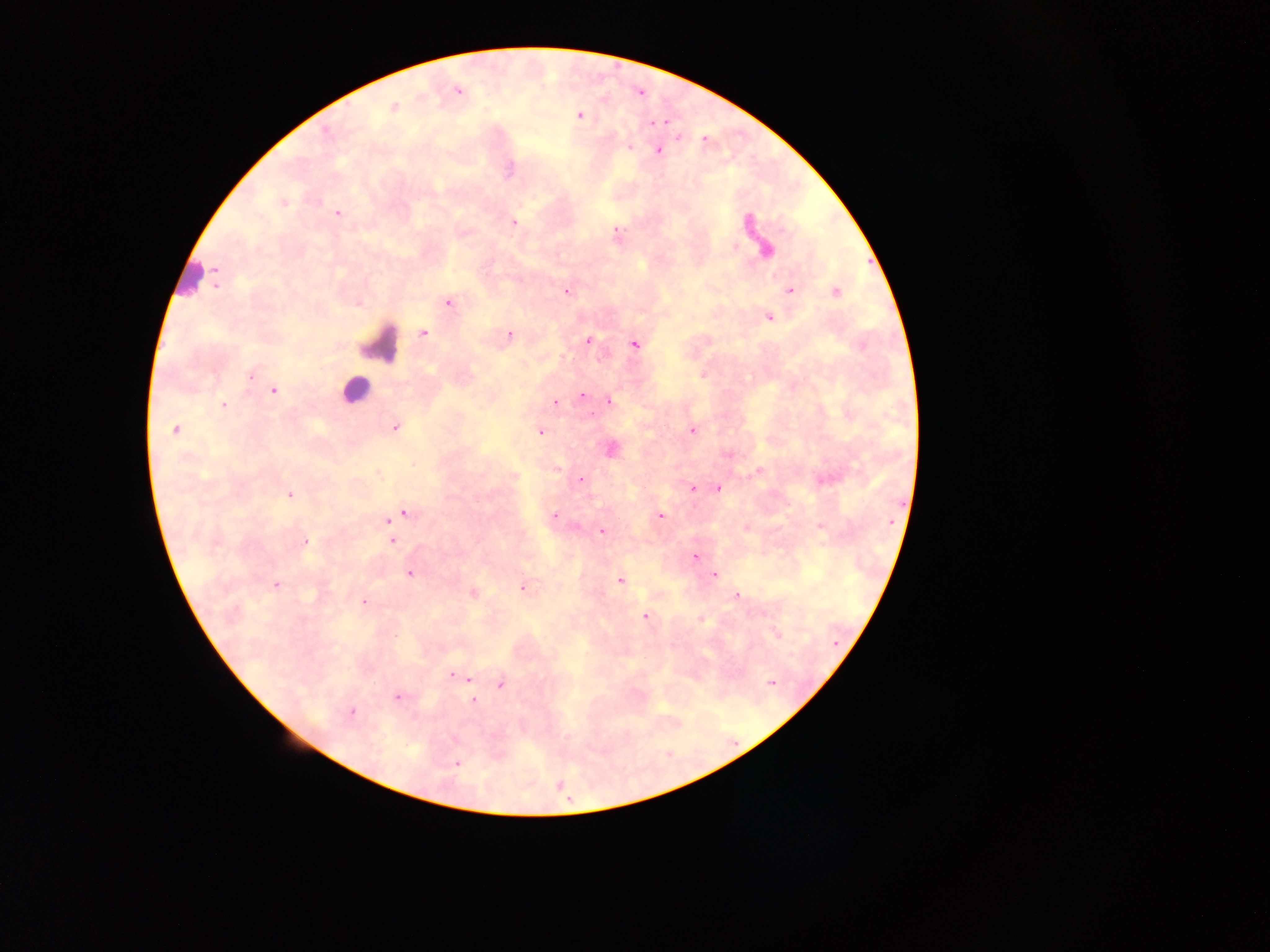

Approximate centers as {x, y} in pixels. Plasmodium parasite locations: {458, 91}, {640, 93}, {394, 107}, {579, 115}, {664, 121}, {629, 147}, {657, 150}, {283, 203}, {338, 213}, {513, 222}, {747, 223}, {735, 246}, {766, 251}, {215, 271}, {566, 291}, {791, 291}, {836, 292}, {448, 302}, {769, 318}, {424, 333}, {509, 334}, {589, 341}, {633, 344}, {250, 376}, {273, 390}, {582, 395}, {609, 401}, {555, 403}, {223, 405}, {395, 427}, {175, 429}, {692, 430}, {541, 432}, {611, 450}, {759, 471}, {580, 479}, {828, 480}, {692, 488}, {718, 489}, {289, 494}, {406, 513}, {555, 516}, {661, 516}, {395, 518}, {387, 520}, {821, 527}, {602, 532}, {304, 541}, {392, 541}, {695, 557}, {410, 574}, {715, 575}, {620, 580}, {276, 585}, {523, 588}, {473, 593}, {737, 595}, {364, 602}, {645, 617}, {700, 619}, {777, 635}, {454, 675}, {770, 683}, {501, 685}, {397, 697}, {473, 700}, {351, 712}, {457, 763}. Leukocyte locations: {190, 279}, {382, 343}, {355, 390}. Collected in Ghana. Photographed through a microscope with a mobile-phone camera. Single field of view. Image is 1270×952 pixels. Thick blood smear.